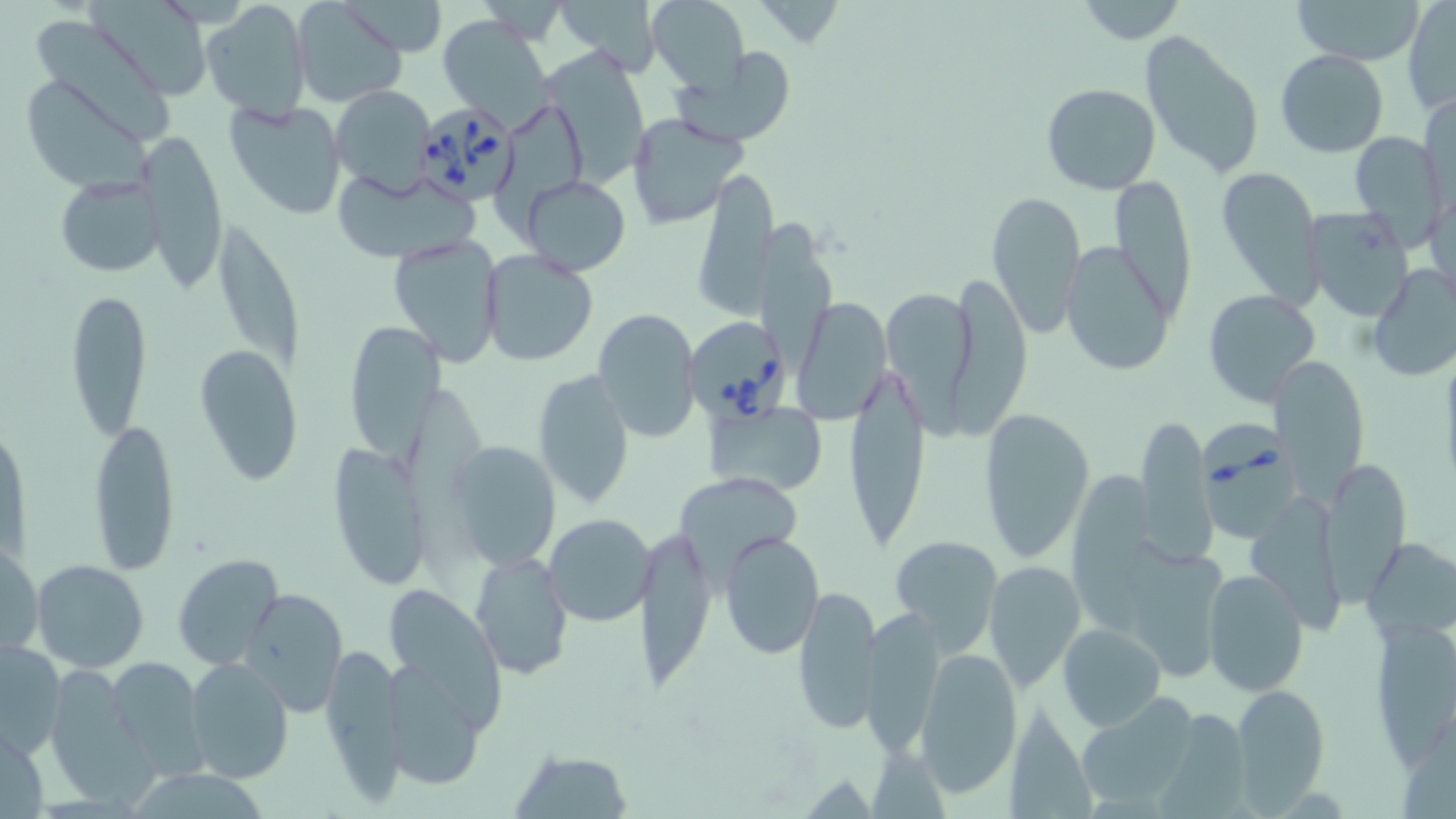
Summary:
  - Coordinate format: approximate bounding boxes as [x1, y1, x2, y2] in pixels
  - Uninfected red blood cell locations: [294, 0, 406, 107], [346, 0, 450, 59], [558, 0, 664, 70], [646, 0, 750, 90], [1073, 0, 1188, 44], [1293, 0, 1424, 65], [1403, 0, 1455, 115], [90, 1, 214, 99], [201, 2, 311, 121], [32, 10, 177, 146], [438, 14, 555, 129], [1139, 32, 1266, 182], [541, 45, 666, 192], [674, 47, 801, 146], [1275, 49, 1389, 158], [20, 74, 150, 192], [1041, 83, 1161, 194], [331, 86, 438, 195], [1420, 90, 1455, 214], [224, 97, 349, 221], [502, 105, 589, 234], [627, 112, 746, 228], [137, 131, 230, 292], [1349, 131, 1445, 249], [1214, 165, 1325, 306], [331, 167, 480, 263], [689, 168, 778, 320], [519, 175, 632, 276], [55, 176, 165, 275], [1109, 176, 1196, 326], [986, 189, 1086, 340], [1302, 207, 1415, 321], [755, 218, 833, 376], [214, 228, 299, 370], [388, 234, 503, 365], [1060, 241, 1175, 377], [480, 250, 598, 366], [1365, 262, 1456, 380], [951, 278, 1028, 440], [66, 287, 152, 442], [1202, 290, 1317, 408], [884, 291, 976, 444], [791, 300, 894, 423], [592, 309, 700, 442], [343, 320, 445, 464], [194, 344, 303, 484], [843, 355, 931, 558], [1270, 355, 1368, 498], [532, 367, 635, 510], [709, 401, 826, 497], [980, 407, 1095, 562], [2, 418, 28, 561], [88, 418, 180, 575], [1135, 418, 1216, 560], [446, 438, 561, 571], [323, 442, 433, 593], [1320, 459, 1409, 601], [673, 470, 806, 583], [1073, 472, 1156, 631], [1248, 496, 1341, 634], [543, 512, 656, 627], [638, 520, 715, 699], [719, 531, 824, 659], [890, 536, 1002, 655], [1364, 537, 1455, 642], [1124, 540, 1229, 681], [1, 544, 44, 655], [471, 551, 572, 678], [173, 554, 284, 671], [32, 560, 151, 672], [985, 560, 1085, 692], [1202, 567, 1309, 696], [794, 583, 880, 736], [240, 587, 349, 715], [386, 593, 506, 735], [862, 609, 946, 760], [1369, 615, 1456, 763], [1059, 623, 1167, 733], [1, 640, 66, 759], [321, 640, 408, 805], [916, 649, 1022, 796], [102, 657, 207, 780], [185, 657, 294, 784], [43, 664, 150, 806], [389, 667, 484, 797], [1231, 683, 1331, 809], [1077, 693, 1205, 813], [1004, 702, 1104, 819], [1158, 711, 1252, 819], [1, 721, 48, 818], [511, 749, 634, 819], [134, 771, 282, 819]
  - Babesia divergens-infected red blood cell locations: [408, 101, 522, 204], [684, 320, 793, 432], [1198, 412, 1301, 547]
  - Slide-level diagnosis: Babesia divergens
  - Image size: 1456×819 pixels
  - Preparation: thin blood smear
  - Modality: optical microscopy
  - Stain: May-Grünwald-Giemsa
  - Magnification: 1000x
  - Field of view: one of a larger specimen